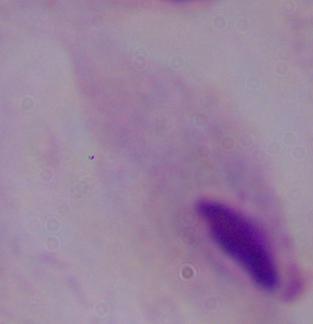
identification = trichomonad
magnification = 1000x
modality = micrograph